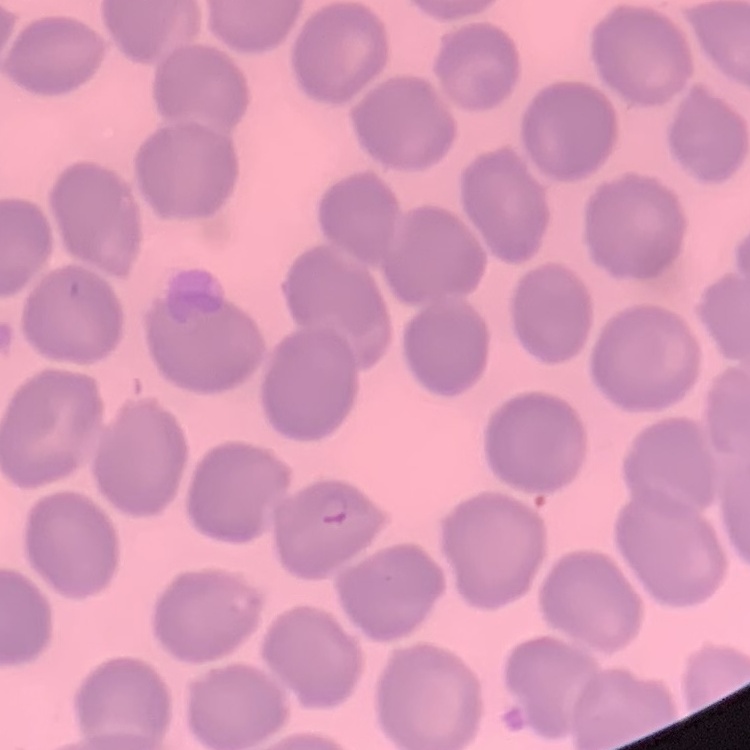
Summary:
  - Red blood cell morphology: no rouleaux formation
  - Image type: square crop of a larger photomicrograph
  - Preparation: thin peripheral smear
  - Stain: Field's or Giemsa